Identify the preparation type.
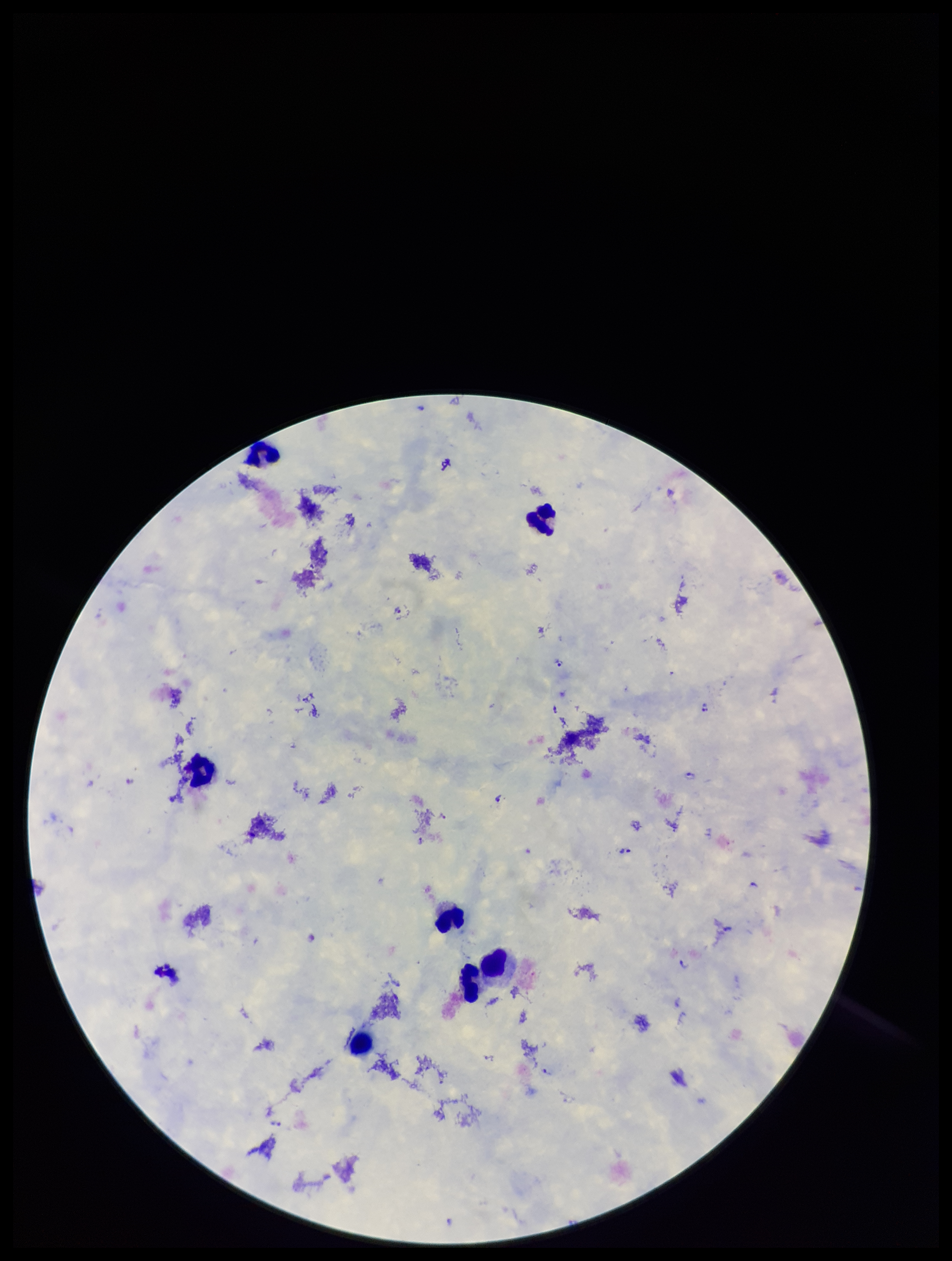

Thick.

Summary:
  - Capture: smartphone photograph through the microscope eyepiece
  - Leukocyte count: 7
  - Patient malaria status: positive
  - Plasmodium parasites: detected
  - Parasite count: 20
  - Image size: 952×1261 pixels
  - Species reported for this patient: Plasmodium falciparum
  - Field of view: single
  - Stain: Giemsa